State which cell type is depicted.
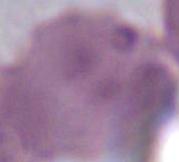

This is an erythrocyte.

magnification = 1000x
modality = photomicrograph